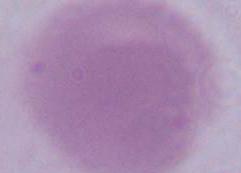

magnification = 1000x
modality = micrograph
identification = red blood cell